Identify the blood parasite species.
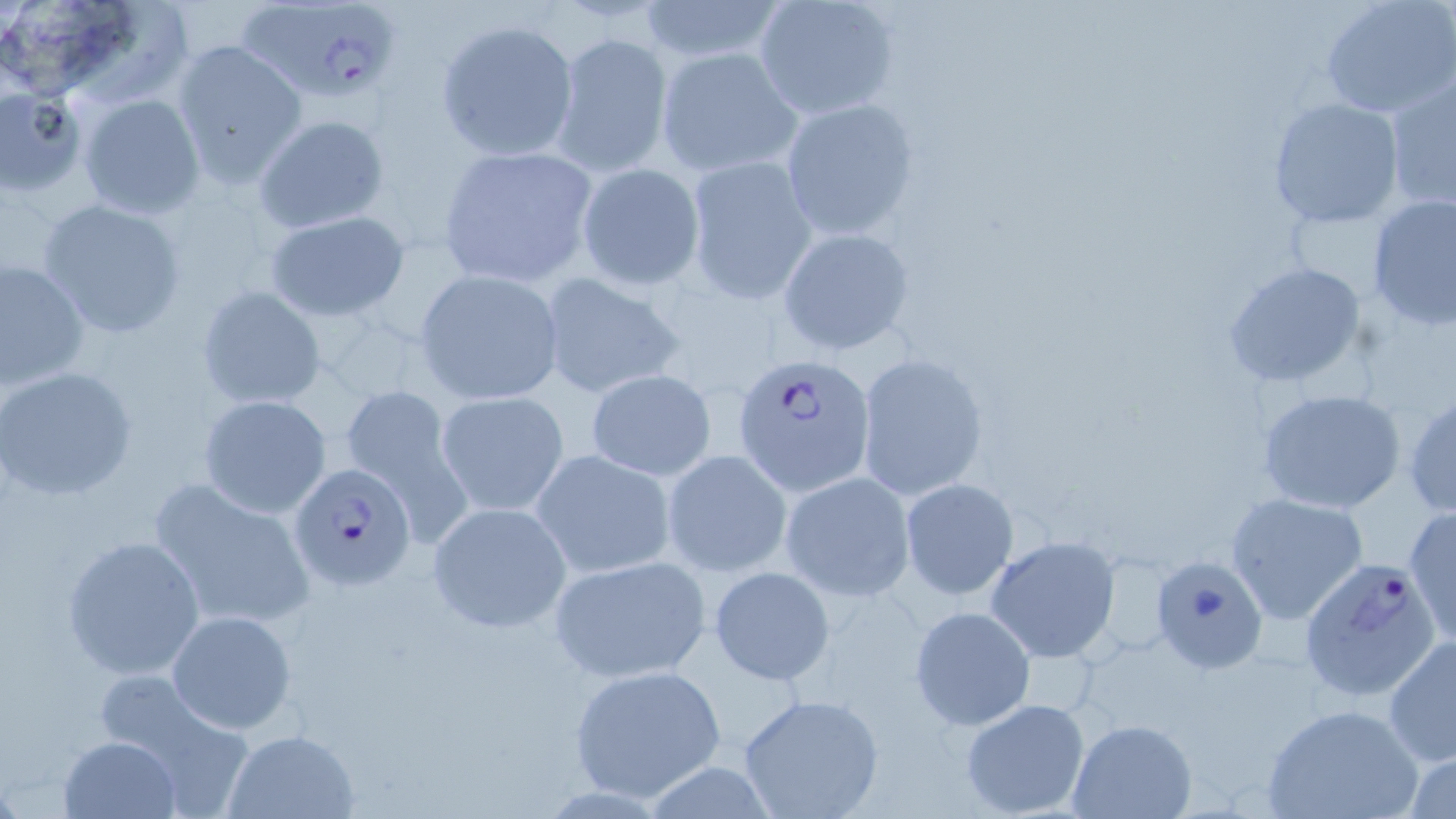
Plasmodium falciparum.

Summary:
  - Coordinate format: approximate bounding boxes as [x1, y1, x2, y2] in pixels
  - Uninfected red blood cell locations: [637, 0, 786, 67], [752, 0, 900, 121], [1319, 0, 1456, 118], [434, 17, 580, 162], [550, 29, 673, 177], [171, 40, 308, 188], [655, 46, 802, 177], [1385, 74, 1455, 212], [0, 84, 87, 197], [75, 92, 206, 219], [1268, 97, 1405, 229], [780, 98, 920, 241], [252, 114, 388, 235], [437, 143, 600, 289], [683, 155, 818, 305], [576, 164, 705, 290], [1366, 194, 1456, 331], [35, 196, 190, 339], [262, 209, 412, 322], [777, 227, 915, 357], [0, 255, 90, 392], [1223, 262, 1368, 387], [414, 269, 564, 404], [537, 270, 686, 400], [197, 285, 325, 410], [856, 351, 989, 500], [0, 366, 138, 502], [583, 369, 717, 482], [336, 379, 471, 532], [1257, 387, 1408, 514], [434, 391, 569, 518], [1405, 391, 1455, 517], [198, 394, 332, 518], [531, 449, 676, 578], [661, 449, 793, 577], [779, 472, 915, 602], [146, 475, 316, 631], [898, 477, 1019, 601], [1225, 490, 1370, 626], [427, 500, 571, 634], [1404, 506, 1455, 648], [61, 534, 204, 680], [984, 536, 1123, 664], [547, 554, 711, 683], [1154, 555, 1267, 674], [708, 565, 835, 685], [909, 605, 1036, 731], [166, 609, 298, 735], [1381, 637, 1456, 767], [568, 663, 728, 802], [89, 676, 256, 815], [738, 693, 885, 819], [958, 698, 1092, 817], [1263, 703, 1422, 819], [1065, 718, 1200, 819], [222, 728, 360, 819], [59, 734, 182, 819], [1402, 744, 1456, 819]
  - Plasmodium falciparum-infected red blood cell locations: [236, 0, 402, 105], [734, 353, 876, 497], [289, 463, 417, 593], [1299, 561, 1444, 703]
  - Preparation: thin blood smear
  - Image size: 1456×819 pixels
  - Modality: optical microscopy
  - Field of view: single
  - Magnification: 1000x
  - Stain: May-Grünwald-Giemsa